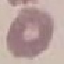

Malaria status: uninfected. Cell patch, automatically extracted from a larger field of view and resized to 64 × 64 pixels. Acquired by smartphone through the microscope eyepiece. Giemsa-stained preparation. Thin blood smear.